Locate every blood parasite and identify its species.
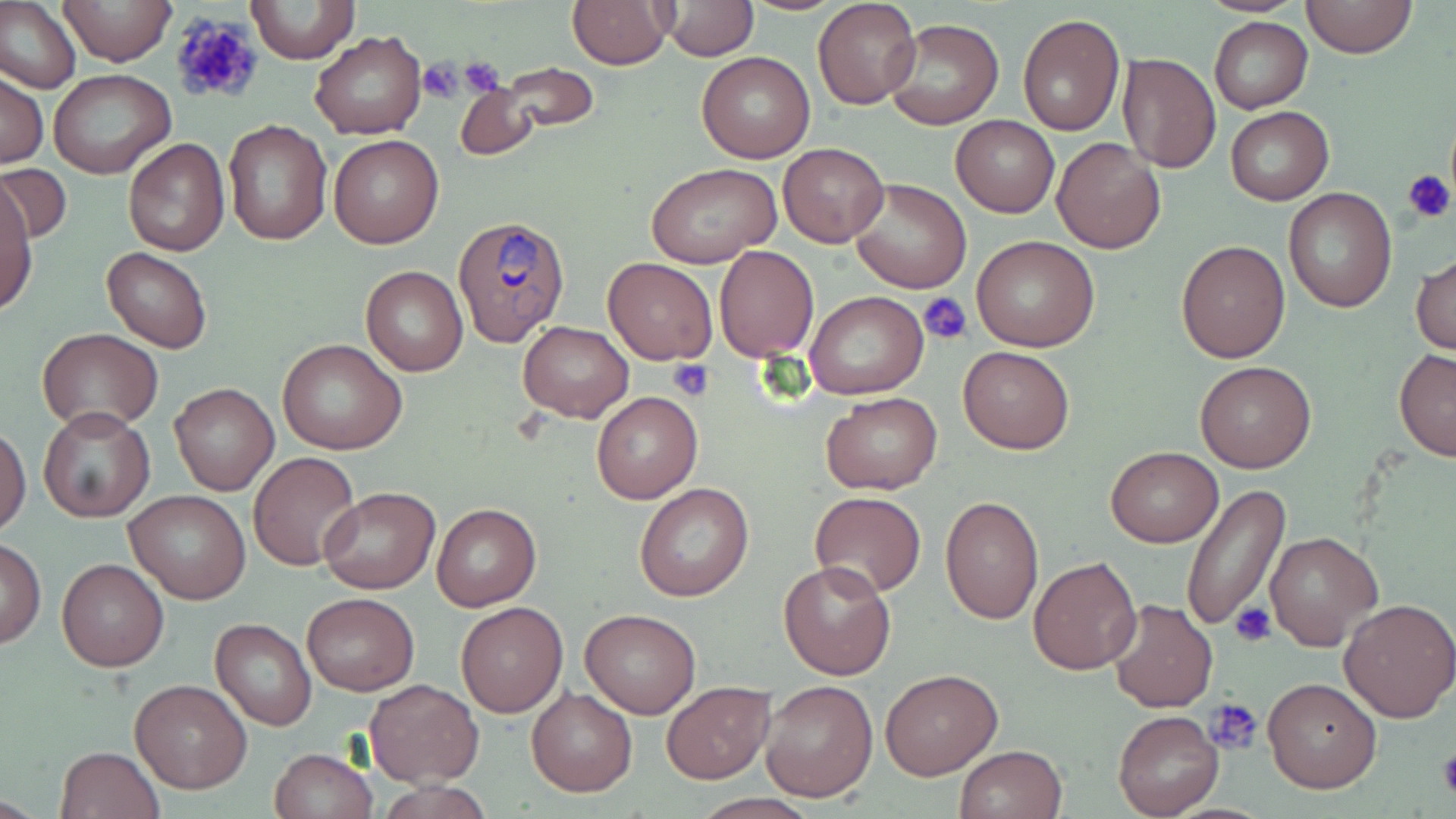

Approximate bounding boxes as [x1, y1, x2, y2] in pixels.
Plasmodium ovale-infected red blood cells: [455, 214, 570, 346].
No Plasmodium falciparum, Plasmodium malariae, Plasmodium vivax, Babesia divergens, or Trypanosoma brucei observed.

Summary:
  - Uninfected red blood cell locations: [0, 0, 80, 95], [57, 0, 178, 66], [245, 0, 360, 65], [663, 0, 756, 60], [813, 0, 922, 108], [1298, 0, 1418, 59], [568, 1, 673, 69], [1017, 14, 1125, 135], [1209, 18, 1312, 113], [883, 20, 1003, 131], [310, 30, 426, 140], [697, 51, 815, 163], [1117, 51, 1221, 175], [484, 63, 601, 135], [50, 69, 175, 180], [0, 71, 49, 168], [454, 81, 539, 160], [1225, 106, 1332, 206], [951, 115, 1058, 218], [223, 119, 333, 246], [329, 135, 443, 248], [122, 137, 230, 256], [1051, 137, 1165, 253], [778, 142, 889, 248], [0, 163, 72, 246], [647, 163, 781, 268], [849, 177, 970, 294], [2, 178, 39, 312], [1283, 189, 1398, 312], [971, 236, 1099, 353], [1176, 240, 1290, 363], [715, 246, 819, 361], [101, 247, 212, 353], [1412, 253, 1455, 357], [602, 256, 718, 365], [360, 266, 467, 376], [804, 290, 929, 401], [518, 321, 633, 421], [37, 329, 164, 432], [278, 339, 406, 456], [957, 346, 1075, 453], [1394, 348, 1456, 461], [1196, 359, 1316, 472], [169, 383, 279, 496], [592, 391, 703, 505], [820, 392, 942, 494], [37, 407, 156, 525], [1, 426, 30, 537], [1105, 446, 1223, 546], [250, 452, 360, 571], [636, 483, 753, 602], [1180, 483, 1291, 633], [318, 486, 438, 594], [125, 491, 250, 605], [810, 491, 926, 598], [939, 496, 1044, 625], [431, 503, 540, 611], [441, 513, 549, 700], [1263, 530, 1382, 652], [1, 539, 47, 647], [1029, 556, 1142, 675], [57, 557, 169, 671], [778, 559, 896, 680], [302, 593, 419, 694], [1106, 599, 1218, 713], [1338, 599, 1456, 722], [455, 603, 568, 717], [579, 609, 702, 718], [210, 617, 316, 731], [879, 667, 1003, 779], [1260, 676, 1382, 792], [364, 678, 484, 785], [129, 679, 253, 793], [759, 679, 878, 803], [661, 682, 774, 783], [526, 686, 638, 796], [1113, 711, 1223, 817], [956, 744, 1068, 819], [55, 746, 165, 819], [269, 747, 376, 818]
  - Platelet locations: [169, 12, 266, 107], [457, 56, 504, 97], [417, 58, 463, 103], [1401, 168, 1455, 223], [918, 291, 973, 347], [667, 359, 713, 400], [1229, 602, 1277, 648], [1208, 699, 1264, 754], [1438, 746, 1456, 799]
  - Slide-level diagnosis: Plasmodium ovale
  - Modality: light microscopy
  - Preparation: thin blood smear
  - Image size: 1456×819 pixels
  - Field of view: single
  - Stain: May-Grünwald-Giemsa
  - Magnification: 1000x